Outline each blood parasite and name the species.
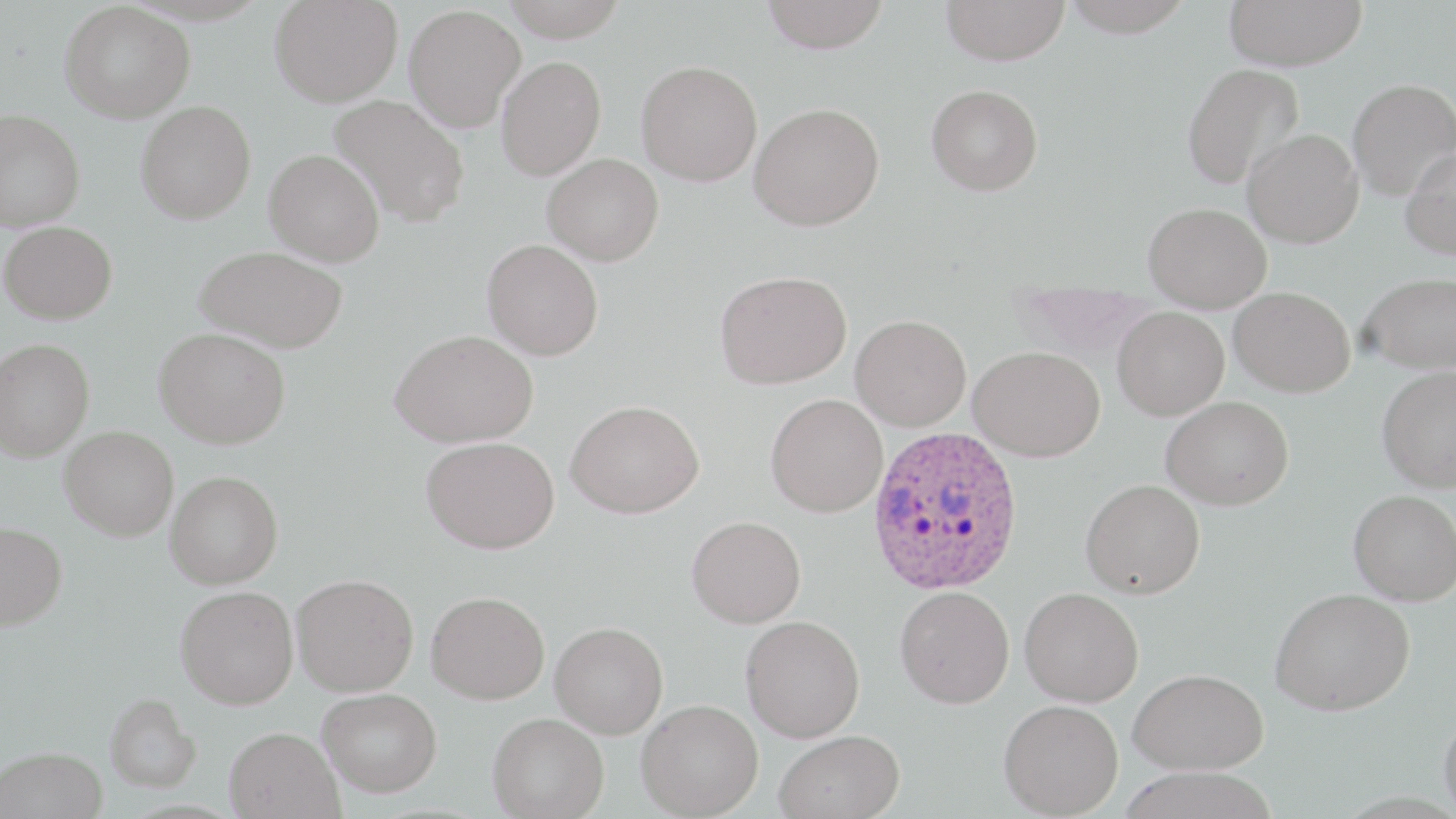
Approximate bounding boxes as named x1/y1/x2/y2 corners in pixels.
Plasmodium ovale-infected red blood cells: (x1=866, y1=425, x2=1025, y2=595).
No Plasmodium falciparum, Plasmodium malariae, Plasmodium vivax, Babesia divergens, or Trypanosoma brucei observed.

Summary:
  - Uninfected red blood cell locations: (x1=269, y1=0, x2=402, y2=107), (x1=500, y1=0, x2=629, y2=41), (x1=761, y1=0, x2=891, y2=54), (x1=941, y1=0, x2=1070, y2=66), (x1=1059, y1=0, x2=1196, y2=37), (x1=1223, y1=0, x2=1368, y2=71), (x1=59, y1=2, x2=195, y2=123), (x1=404, y1=4, x2=525, y2=132), (x1=496, y1=56, x2=606, y2=180), (x1=636, y1=60, x2=763, y2=186), (x1=1182, y1=63, x2=1304, y2=190), (x1=1347, y1=78, x2=1456, y2=200), (x1=926, y1=84, x2=1043, y2=195), (x1=330, y1=95, x2=470, y2=228), (x1=135, y1=101, x2=256, y2=224), (x1=749, y1=103, x2=885, y2=231), (x1=0, y1=109, x2=85, y2=232), (x1=1242, y1=128, x2=1363, y2=248), (x1=1400, y1=146, x2=1456, y2=260), (x1=264, y1=148, x2=384, y2=267), (x1=542, y1=153, x2=664, y2=265), (x1=1143, y1=202, x2=1271, y2=311), (x1=1, y1=221, x2=117, y2=324), (x1=482, y1=239, x2=603, y2=360), (x1=195, y1=245, x2=348, y2=353), (x1=715, y1=270, x2=851, y2=389), (x1=1359, y1=272, x2=1456, y2=374), (x1=1229, y1=286, x2=1355, y2=397), (x1=1113, y1=307, x2=1229, y2=420), (x1=850, y1=314, x2=971, y2=431), (x1=153, y1=327, x2=291, y2=449), (x1=389, y1=329, x2=538, y2=447), (x1=0, y1=336, x2=94, y2=462), (x1=968, y1=346, x2=1105, y2=462), (x1=1376, y1=365, x2=1456, y2=492), (x1=765, y1=394, x2=888, y2=517), (x1=1161, y1=396, x2=1294, y2=509), (x1=566, y1=399, x2=704, y2=518), (x1=60, y1=425, x2=178, y2=540), (x1=421, y1=436, x2=559, y2=554), (x1=165, y1=470, x2=283, y2=589), (x1=1080, y1=479, x2=1205, y2=599), (x1=1349, y1=489, x2=1456, y2=605), (x1=686, y1=515, x2=806, y2=628), (x1=0, y1=521, x2=67, y2=630), (x1=291, y1=573, x2=419, y2=696), (x1=175, y1=585, x2=298, y2=709), (x1=895, y1=586, x2=1014, y2=708), (x1=1020, y1=587, x2=1144, y2=707), (x1=1269, y1=587, x2=1414, y2=715), (x1=426, y1=590, x2=549, y2=703), (x1=741, y1=615, x2=865, y2=742), (x1=550, y1=621, x2=669, y2=738), (x1=1128, y1=667, x2=1268, y2=774), (x1=317, y1=687, x2=442, y2=797), (x1=105, y1=693, x2=202, y2=792), (x1=636, y1=699, x2=763, y2=818), (x1=999, y1=699, x2=1124, y2=818), (x1=1438, y1=709, x2=1456, y2=819), (x1=487, y1=712, x2=609, y2=818), (x1=224, y1=726, x2=345, y2=818), (x1=774, y1=729, x2=905, y2=819), (x1=1, y1=747, x2=107, y2=819), (x1=1117, y1=766, x2=1281, y2=819)
  - Slide-level diagnosis: Plasmodium ovale
  - Image size: 1456×819 pixels
  - Magnification: 1000x
  - Stain: May-Grünwald-Giemsa
  - Preparation: thin blood film
  - Field of view: single
  - Modality: light microscopy